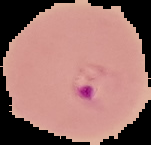
Summary:
  - Result: Plasmodium parasites identified
  - Preparation: thin blood film
  - Image type: cell region segmented out of the field of view; surrounding area masked to black
  - Image size: 151×145 pixels